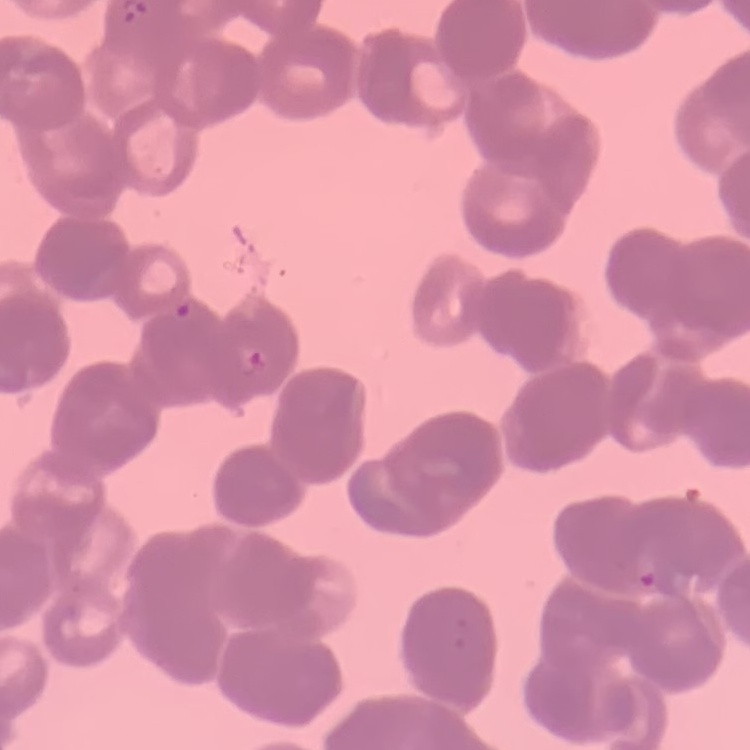

Summary:
  - Erythrocyte morphology: rouleaux formation
  - Stain: Field's or Giemsa
  - Image type: square crop of a larger photomicrograph
  - Preparation: thin peripheral smear